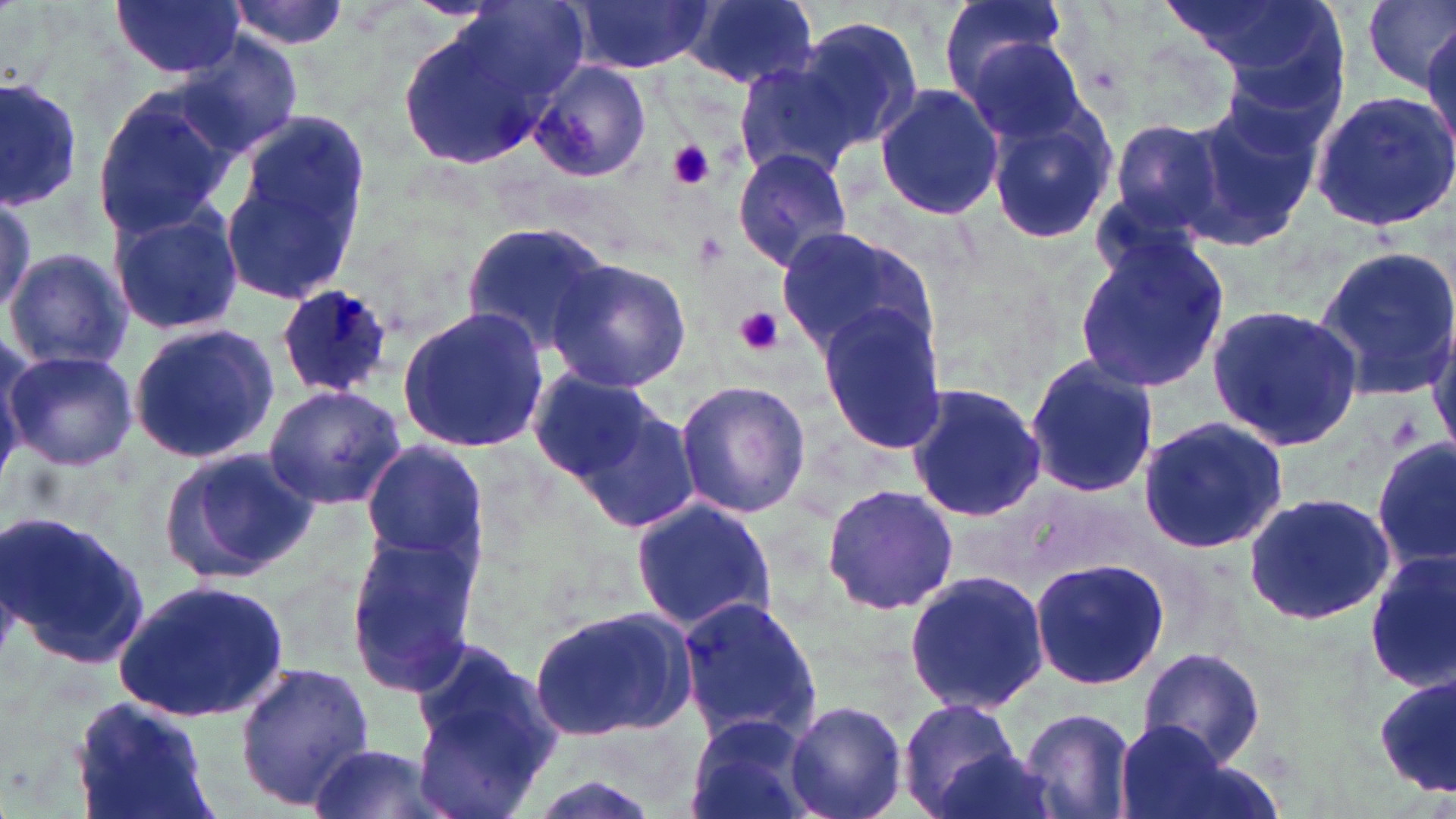

Summary:
  - Coordinate format: approximate bounding boxes as (x1,y1)-(x2,y2) corner pairs in pixels
  - Plasmodium ovale-infected red blood cell locations: (277,285)-(397,398)
  - Platelet locations: (666,141)-(716,191), (733,306)-(784,357)
  - Uninfected red blood cell locations: (225,0)-(352,52), (685,0)-(818,89), (936,0)-(1074,110), (1360,0)-(1456,91), (112,1)-(241,79), (571,1)-(711,74), (1165,1)-(1337,75), (394,7)-(576,166), (792,16)-(922,153), (1421,22)-(1456,159), (960,32)-(1092,148), (176,33)-(301,158), (731,57)-(860,181), (528,62)-(652,185), (0,77)-(87,212), (873,85)-(1004,218), (89,90)-(237,244), (1307,92)-(1456,234), (1183,99)-(1322,248), (985,104)-(1120,246), (220,113)-(370,305), (1107,115)-(1236,242), (731,146)-(853,272), (0,187)-(36,316), (108,203)-(245,337), (460,222)-(615,356), (775,226)-(939,360), (1073,233)-(1235,396), (1312,245)-(1456,401), (5,246)-(136,372), (548,257)-(694,393), (1205,303)-(1364,452), (816,306)-(948,454), (397,307)-(551,455), (127,323)-(280,465), (4,350)-(140,471), (1024,353)-(1160,501), (533,366)-(659,483), (675,379)-(811,518), (904,380)-(1048,524), (263,384)-(407,509), (571,398)-(703,535), (1136,415)-(1289,555), (1372,438)-(1455,572), (362,443)-(489,562), (158,447)-(318,584), (819,482)-(958,615), (1244,489)-(1398,626), (628,497)-(777,635), (0,511)-(152,673), (339,533)-(480,698), (1363,551)-(1455,690), (1028,556)-(1172,692), (903,568)-(1051,712), (112,579)-(293,724), (674,592)-(822,748), (527,604)-(701,741), (408,638)-(558,810), (1135,648)-(1267,769), (235,661)-(374,806), (1376,673)-(1454,796), (73,695)-(222,819), (897,698)-(1029,819), (787,701)-(908,819), (1018,706)-(1136,819), (682,713)-(820,819), (1113,719)-(1244,819), (306,741)-(451,819), (923,744)-(1062,819)
  - Slide-level diagnosis: Plasmodium ovale
  - Modality: optical microscopy
  - Magnification: 1000x
  - Preparation: thin blood film
  - Stain: May-Grünwald-Giemsa
  - Field of view: single
  - Image size: 1456×819 pixels